Assess this cell for malaria.
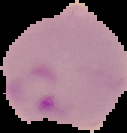

Parasitized.

Image is 127×133 pixels. From a thin blood film. The area outside the segmented cell region is set to black.